Assess this cell for malaria.
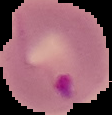
Parasitized.

Summary:
  - Preparation: thin blood smear
  - Image type: cell region segmented out of the field of view; surrounding area masked to black
  - Image size: 112×115 pixels